State which parasite is depicted.
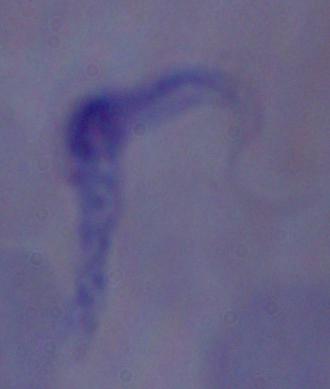

This is a trypanosome.

magnification = 1000x
modality = micrograph